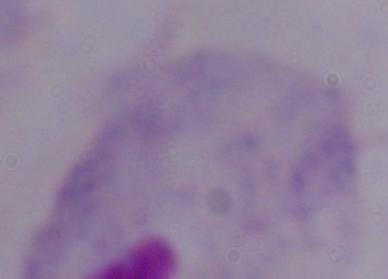
Summary:
  - Modality: micrograph
  - Magnification: 1000x
  - Identification: trichomonad